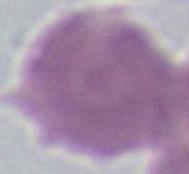

Micrograph. An erythrocyte is seen. Captured at 1000x magnification.